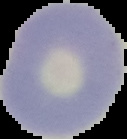

image type = cell region segmented out of the field of view; surrounding area masked to black
preparation = thin blood smear
image size = 127×139 pixels
malaria status = uninfected